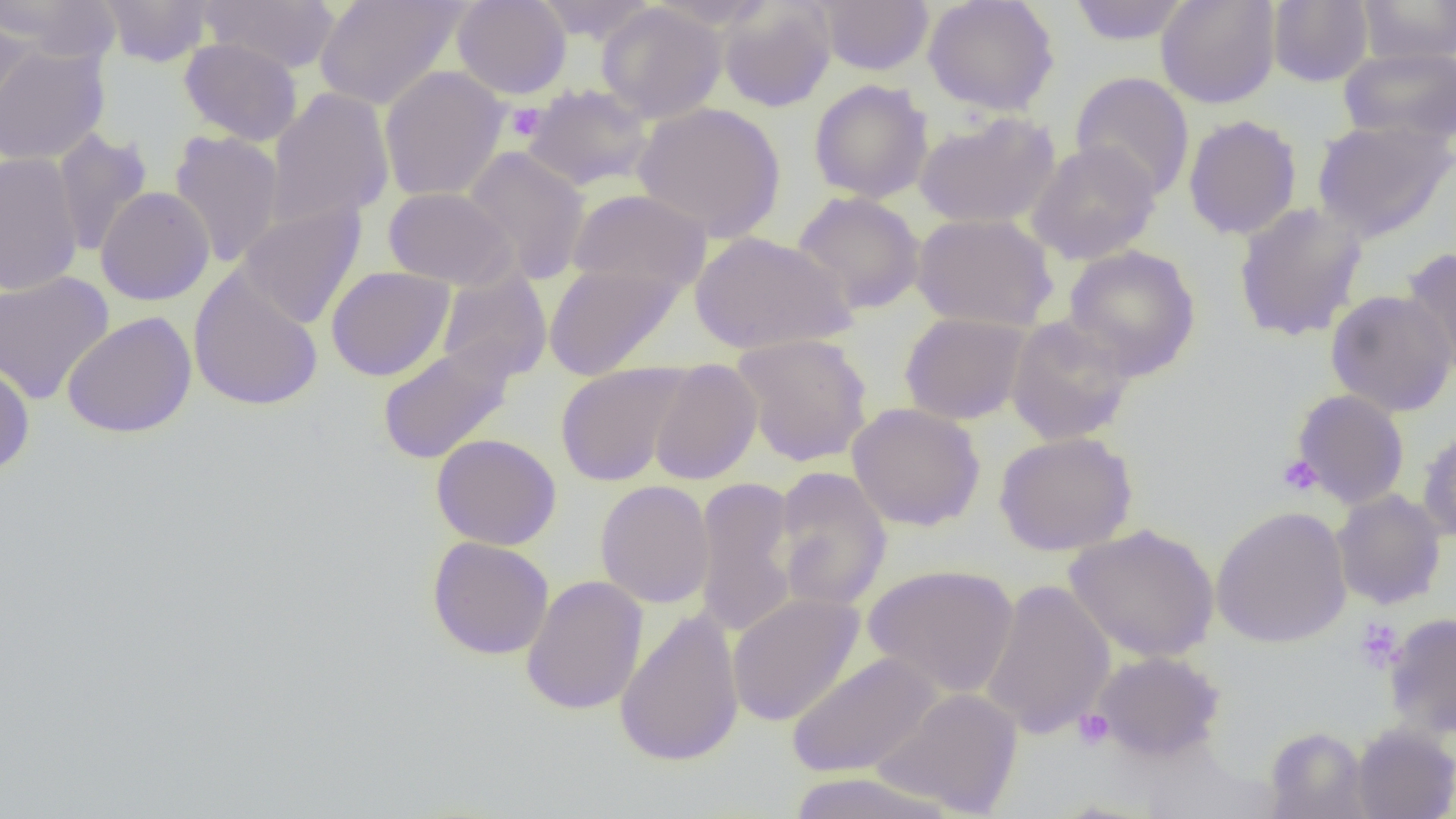

Approximate bounding boxes as named x1/y1/x2/y2 corners in pixels. Uninfected red blood cell locations: (x1=1, y1=0, x2=122, y2=64), (x1=98, y1=0, x2=214, y2=67), (x1=200, y1=0, x2=340, y2=74), (x1=314, y1=0, x2=469, y2=112), (x1=452, y1=0, x2=572, y2=99), (x1=534, y1=0, x2=659, y2=43), (x1=815, y1=0, x2=935, y2=75), (x1=923, y1=0, x2=1060, y2=116), (x1=1156, y1=0, x2=1280, y2=109), (x1=1267, y1=0, x2=1373, y2=87), (x1=1356, y1=0, x2=1456, y2=65), (x1=717, y1=1, x2=836, y2=112), (x1=1067, y1=1, x2=1192, y2=45), (x1=596, y1=3, x2=727, y2=123), (x1=0, y1=10, x2=35, y2=126), (x1=179, y1=37, x2=303, y2=146), (x1=0, y1=43, x2=110, y2=166), (x1=1338, y1=46, x2=1456, y2=147), (x1=379, y1=66, x2=509, y2=202), (x1=1070, y1=71, x2=1195, y2=202), (x1=809, y1=79, x2=933, y2=204), (x1=523, y1=84, x2=654, y2=192), (x1=266, y1=87, x2=395, y2=229), (x1=632, y1=102, x2=786, y2=242), (x1=913, y1=111, x2=1061, y2=230), (x1=1183, y1=114, x2=1302, y2=240), (x1=1311, y1=117, x2=1456, y2=243), (x1=52, y1=129, x2=153, y2=257), (x1=169, y1=130, x2=285, y2=268), (x1=1026, y1=141, x2=1162, y2=265), (x1=462, y1=146, x2=590, y2=285), (x1=0, y1=152, x2=84, y2=296), (x1=95, y1=186, x2=215, y2=306), (x1=384, y1=187, x2=517, y2=290), (x1=567, y1=188, x2=712, y2=294), (x1=792, y1=191, x2=926, y2=315), (x1=1233, y1=201, x2=1368, y2=342), (x1=237, y1=202, x2=365, y2=330), (x1=911, y1=212, x2=1059, y2=332), (x1=690, y1=230, x2=857, y2=355), (x1=1062, y1=244, x2=1201, y2=380), (x1=1400, y1=247, x2=1456, y2=379), (x1=544, y1=263, x2=684, y2=381), (x1=326, y1=266, x2=455, y2=382), (x1=189, y1=269, x2=323, y2=412), (x1=0, y1=271, x2=114, y2=406), (x1=437, y1=271, x2=552, y2=384), (x1=1325, y1=289, x2=1456, y2=417), (x1=62, y1=311, x2=198, y2=438), (x1=899, y1=312, x2=1032, y2=425), (x1=1005, y1=315, x2=1137, y2=446), (x1=732, y1=333, x2=873, y2=466), (x1=377, y1=342, x2=516, y2=465), (x1=647, y1=359, x2=762, y2=485), (x1=0, y1=362, x2=35, y2=477), (x1=555, y1=362, x2=691, y2=487), (x1=1292, y1=389, x2=1410, y2=509), (x1=847, y1=403, x2=986, y2=532), (x1=1417, y1=426, x2=1456, y2=543), (x1=994, y1=431, x2=1138, y2=556), (x1=431, y1=433, x2=562, y2=551), (x1=772, y1=467, x2=893, y2=612), (x1=691, y1=477, x2=800, y2=639), (x1=595, y1=480, x2=715, y2=609), (x1=1331, y1=489, x2=1447, y2=609), (x1=1211, y1=505, x2=1352, y2=649), (x1=1064, y1=523, x2=1220, y2=663), (x1=427, y1=536, x2=554, y2=660), (x1=862, y1=564, x2=1020, y2=699), (x1=520, y1=574, x2=648, y2=715), (x1=979, y1=579, x2=1115, y2=739), (x1=727, y1=592, x2=865, y2=727), (x1=614, y1=606, x2=745, y2=769), (x1=1383, y1=612, x2=1456, y2=740), (x1=1091, y1=650, x2=1225, y2=763), (x1=786, y1=651, x2=942, y2=779), (x1=872, y1=688, x2=1024, y2=816), (x1=1350, y1=723, x2=1456, y2=819), (x1=1263, y1=726, x2=1371, y2=819), (x1=782, y1=772, x2=957, y2=819). Platelet locations: (x1=506, y1=104, x2=545, y2=141), (x1=1277, y1=455, x2=1323, y2=496), (x1=1355, y1=618, x2=1404, y2=672), (x1=1073, y1=709, x2=1114, y2=750). Slide-level diagnosis: negative for blood parasites. Optical microscopy. 1000x magnification. Image is 1456×819 pixels. Thin blood smear. Single field of view.